Classify this cell by malaria status.
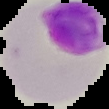

Parasitized.

From a thin blood film. Image is 109×109 pixels. Cell region segmented out of the field of view; the surrounding area is masked to black.